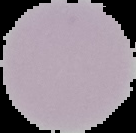
{
  "image_size": "136×133 pixels",
  "result": "no malaria parasites seen",
  "preparation": "thin blood smear",
  "image_type": "segmented cell region with the area outside set to black"
}